Classify this cell by malaria status.
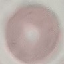

It is uninfected.

Summary:
  - Stain: Giemsa
  - Capture: smartphone through the microscope eyepiece
  - Preparation: thin smear
  - Image type: automatically extracted cell patch, resized to 64 × 64 pixels